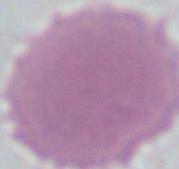
magnification: 1000x
modality: micrograph
identification: erythrocyte